Locate Plasmodium parasites and leukocytes.
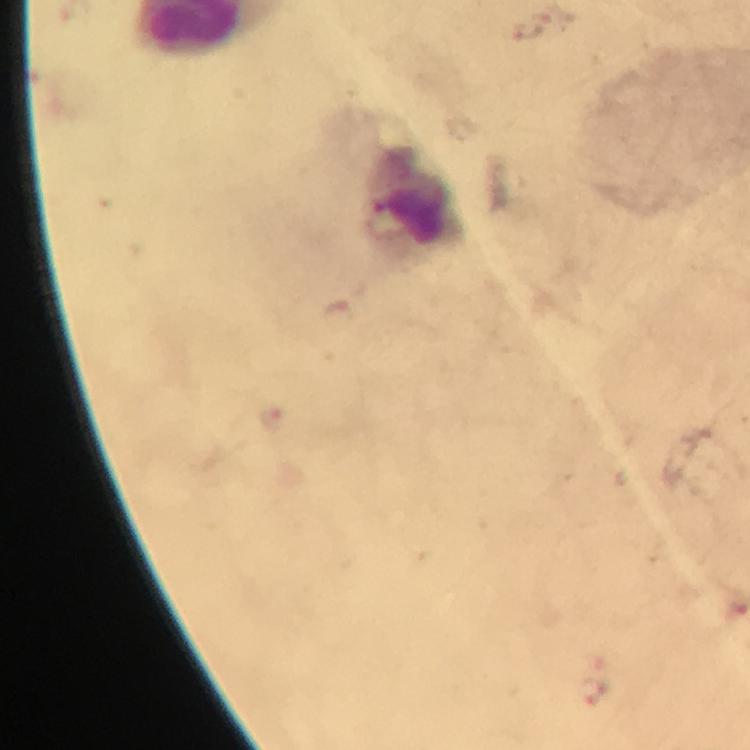
No Plasmodium parasites detected.
Approximate centers as [x, y] in pixels.
Leukocytes: [409, 197].

Summary:
  - Cropped from: one field of view
  - Context: from a diagnostic examination for malaria
  - Capture: smartphone camera through the microscope
  - Immersion oil: used
  - Magnification: 100x
  - Preparation: thick blood smear
  - Image size: 750×750 pixels
  - Stain: Giemsa